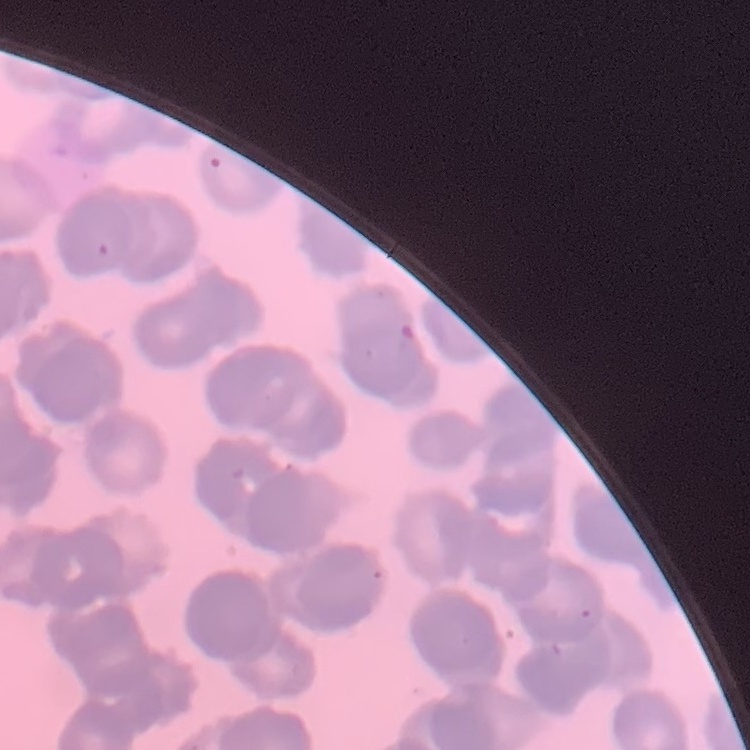
Summary:
  - Erythrocyte morphology: rouleaux formation
  - Preparation: thin peripheral smear
  - Image type: square crop of a larger photomicrograph
  - Stain: Field's or Giemsa